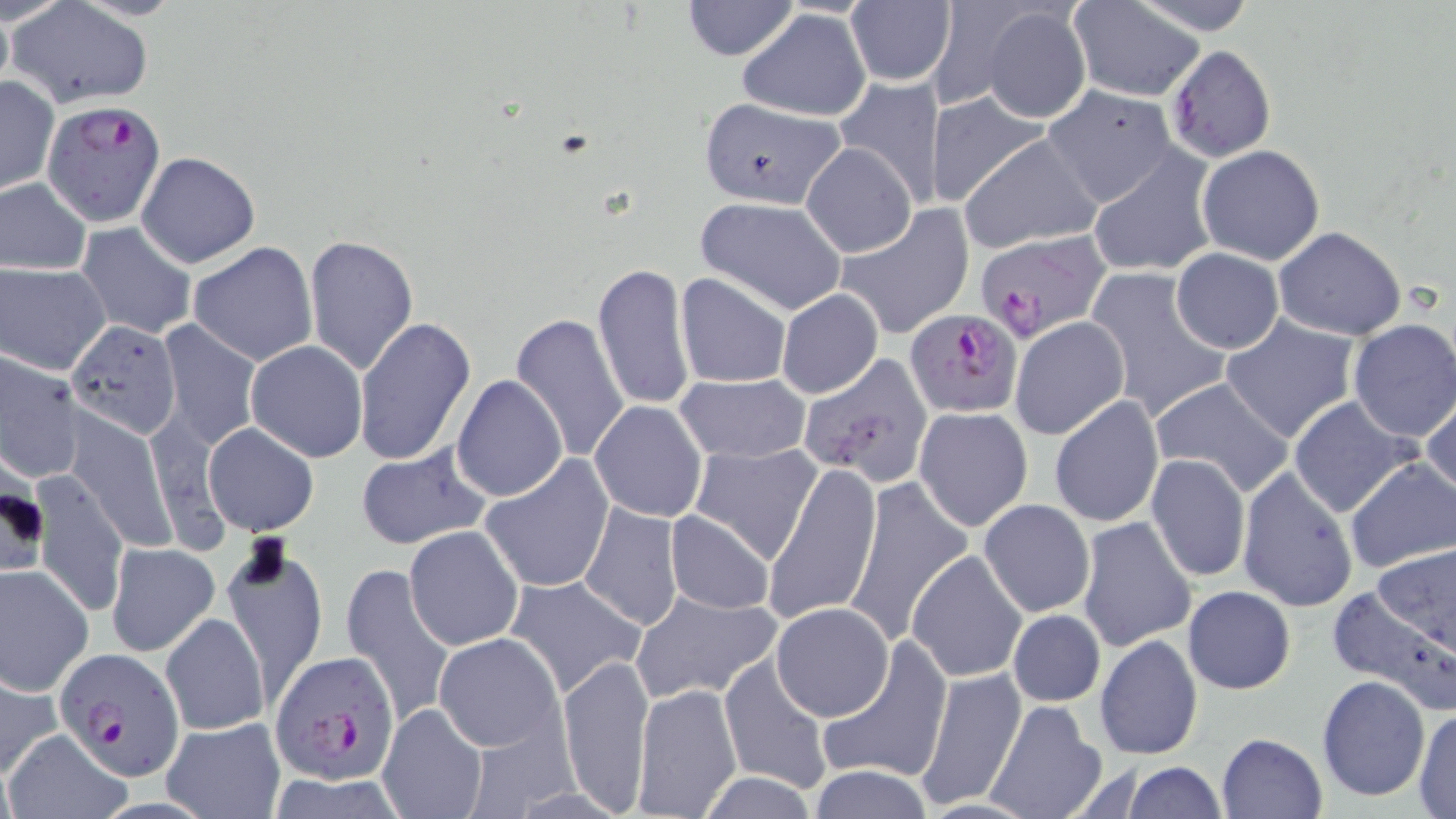

Summary:
  - Coordinate format: approximate bounding boxes as [x1, y1, x2, y2] in pixels
  - Uninfected red blood cell locations: [680, 0, 800, 62], [1070, 0, 1205, 100], [1132, 0, 1260, 33], [8, 2, 154, 109], [0, 3, 13, 97], [845, 3, 956, 86], [921, 3, 1043, 111], [979, 5, 1091, 125], [738, 8, 871, 122], [1165, 45, 1276, 162], [835, 75, 945, 208], [1, 76, 59, 194], [1043, 86, 1177, 207], [926, 91, 1051, 205], [696, 97, 849, 210], [957, 132, 1103, 253], [801, 142, 917, 257], [1196, 145, 1326, 266], [1089, 150, 1218, 278], [137, 151, 258, 268], [0, 178, 92, 275], [696, 196, 849, 315], [832, 205, 975, 340], [78, 222, 197, 338], [1273, 226, 1407, 342], [302, 234, 418, 378], [188, 242, 318, 366], [1170, 248, 1284, 354], [592, 261, 693, 412], [1, 262, 110, 375], [1087, 268, 1232, 424], [676, 273, 791, 389], [777, 289, 884, 398], [510, 312, 631, 464], [1220, 314, 1359, 443], [354, 315, 476, 467], [1010, 317, 1129, 439], [65, 319, 183, 438], [157, 319, 262, 451], [1347, 319, 1456, 441], [245, 340, 367, 462], [0, 353, 83, 483], [798, 355, 935, 487], [451, 373, 567, 503], [675, 374, 810, 463], [1147, 377, 1295, 499], [1421, 395, 1455, 504], [1049, 396, 1163, 528], [1288, 397, 1422, 518], [589, 401, 708, 521], [915, 407, 1035, 532], [65, 409, 175, 553], [144, 409, 230, 555], [203, 422, 319, 537], [688, 442, 822, 563], [354, 445, 491, 552], [479, 454, 615, 595], [1145, 455, 1251, 582], [1346, 459, 1455, 573], [767, 464, 881, 626], [1236, 466, 1360, 613], [32, 468, 129, 619], [841, 477, 971, 651], [979, 498, 1094, 617], [579, 503, 684, 630], [664, 510, 775, 615], [1076, 515, 1197, 652], [404, 525, 524, 650], [219, 541, 327, 704], [107, 542, 220, 656], [364, 543, 507, 703], [1371, 544, 1455, 654], [907, 549, 1029, 683], [339, 562, 458, 729], [0, 563, 94, 694], [502, 573, 645, 698], [1326, 585, 1456, 710], [1183, 587, 1295, 694], [631, 590, 782, 705], [769, 602, 894, 721], [1008, 610, 1106, 707], [160, 613, 270, 735], [434, 632, 564, 751], [1095, 634, 1203, 760], [813, 637, 952, 786], [559, 650, 656, 815], [717, 653, 832, 796], [917, 667, 1026, 811], [0, 672, 58, 778], [1317, 674, 1431, 802], [631, 684, 742, 818], [986, 699, 1108, 819], [377, 702, 489, 819], [1412, 708, 1456, 817], [160, 717, 286, 819], [0, 728, 132, 819], [1217, 733, 1326, 818], [1119, 762, 1226, 818], [806, 765, 935, 819], [692, 772, 822, 818]
  - Plasmodium falciparum-infected red blood cell locations: [42, 101, 166, 228], [964, 228, 1119, 349], [905, 309, 1021, 419], [57, 647, 183, 777], [270, 649, 401, 784]
  - Slide-level diagnosis: Plasmodium falciparum
  - Preparation: thin blood film
  - Magnification: 1000x
  - Modality: optical microscopy
  - Image size: 1456×819 pixels
  - Field of view: single
  - Stain: May-Grünwald-Giemsa